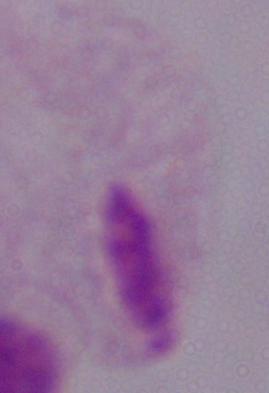

{
  "magnification": "1000x",
  "modality": "photomicrograph",
  "identification": "trichomonad"
}